Assess this cell for malaria.
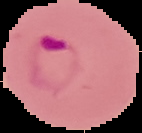
It is parasitized.

From a thin blood smear. The area outside the segmented cell region is set to black. Image is 142×133 pixels.